Identify the blood parasite species.
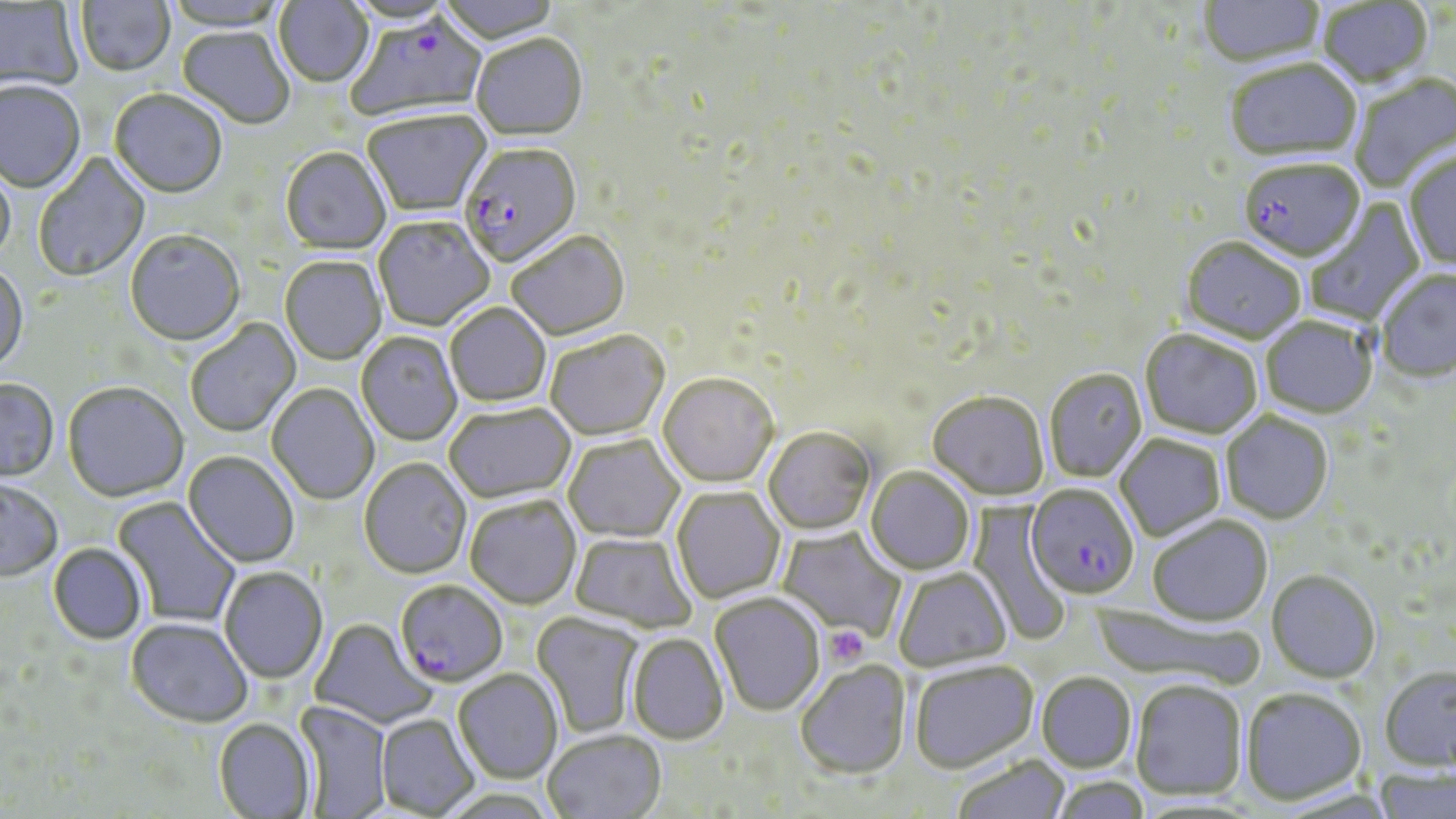
Plasmodium falciparum.

Summary:
  - Coordinate format: approximate bounding boxes as (x1, y1, x2, y2) in pixels
  - Platelet locations: (827, 626, 868, 666)
  - Plasmodium falciparum-infected red blood cell locations: (347, 16, 487, 122), (459, 145, 582, 269), (1238, 160, 1365, 263), (1026, 484, 1139, 599), (395, 580, 508, 688)
  - Uninfected red blood cell locations: (76, 0, 175, 78), (163, 0, 290, 33), (274, 0, 374, 89), (437, 0, 562, 47), (1197, 0, 1325, 69), (0, 1, 83, 93), (1318, 2, 1435, 89), (176, 28, 295, 130), (471, 36, 588, 144), (1225, 61, 1362, 164), (1349, 74, 1456, 193), (0, 83, 85, 194), (109, 91, 227, 200), (363, 112, 492, 219), (280, 149, 391, 256), (1404, 150, 1456, 272), (32, 152, 150, 283), (0, 161, 15, 268), (1305, 197, 1426, 328), (374, 218, 494, 332), (125, 231, 245, 347), (507, 233, 631, 341), (1180, 238, 1306, 344), (279, 257, 386, 365), (0, 264, 28, 376), (1375, 268, 1456, 382), (445, 304, 552, 408), (1260, 316, 1377, 418), (186, 318, 302, 438), (1139, 329, 1262, 439), (546, 332, 669, 441), (356, 333, 462, 446), (1044, 368, 1148, 482), (657, 374, 779, 489), (0, 379, 59, 483), (62, 383, 189, 503), (266, 384, 379, 505), (927, 391, 1050, 500), (444, 404, 576, 503), (1221, 412, 1334, 524), (763, 427, 876, 535), (564, 434, 684, 543), (1115, 434, 1225, 542), (183, 452, 299, 568), (359, 459, 472, 579), (865, 466, 975, 575), (0, 480, 63, 582), (671, 486, 785, 604), (112, 496, 241, 629), (465, 496, 581, 609), (968, 505, 1074, 647), (1147, 515, 1273, 626), (777, 526, 907, 642), (570, 533, 696, 634), (48, 543, 148, 644), (219, 567, 328, 684), (893, 568, 1012, 671), (1267, 569, 1380, 683), (709, 594, 826, 717), (531, 613, 644, 738), (125, 618, 253, 728), (310, 619, 438, 731), (627, 634, 729, 745), (910, 660, 1039, 772), (795, 661, 913, 781), (1379, 666, 1455, 771), (453, 670, 563, 783), (1037, 671, 1137, 772), (1129, 679, 1248, 801), (1241, 686, 1368, 805), (295, 701, 390, 818), (376, 714, 479, 817), (213, 718, 317, 818), (542, 730, 666, 819), (951, 755, 1071, 819), (1373, 767, 1455, 819), (1051, 776, 1151, 819)
  - Field of view: single
  - Modality: light microscopy
  - Preparation: thin blood film
  - Stain: May-Grünwald-Giemsa
  - Image size: 1456×819 pixels
  - Magnification: 1000x